Assess this cell for malaria.
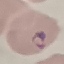
It is parasitized.

Summary:
  - Capture: smartphone camera at the microscope eyepiece
  - Image type: cell patch, automatically extracted from a larger field of view and resized to 64 × 64 pixels
  - Stain: Giemsa
  - Preparation: thin smear